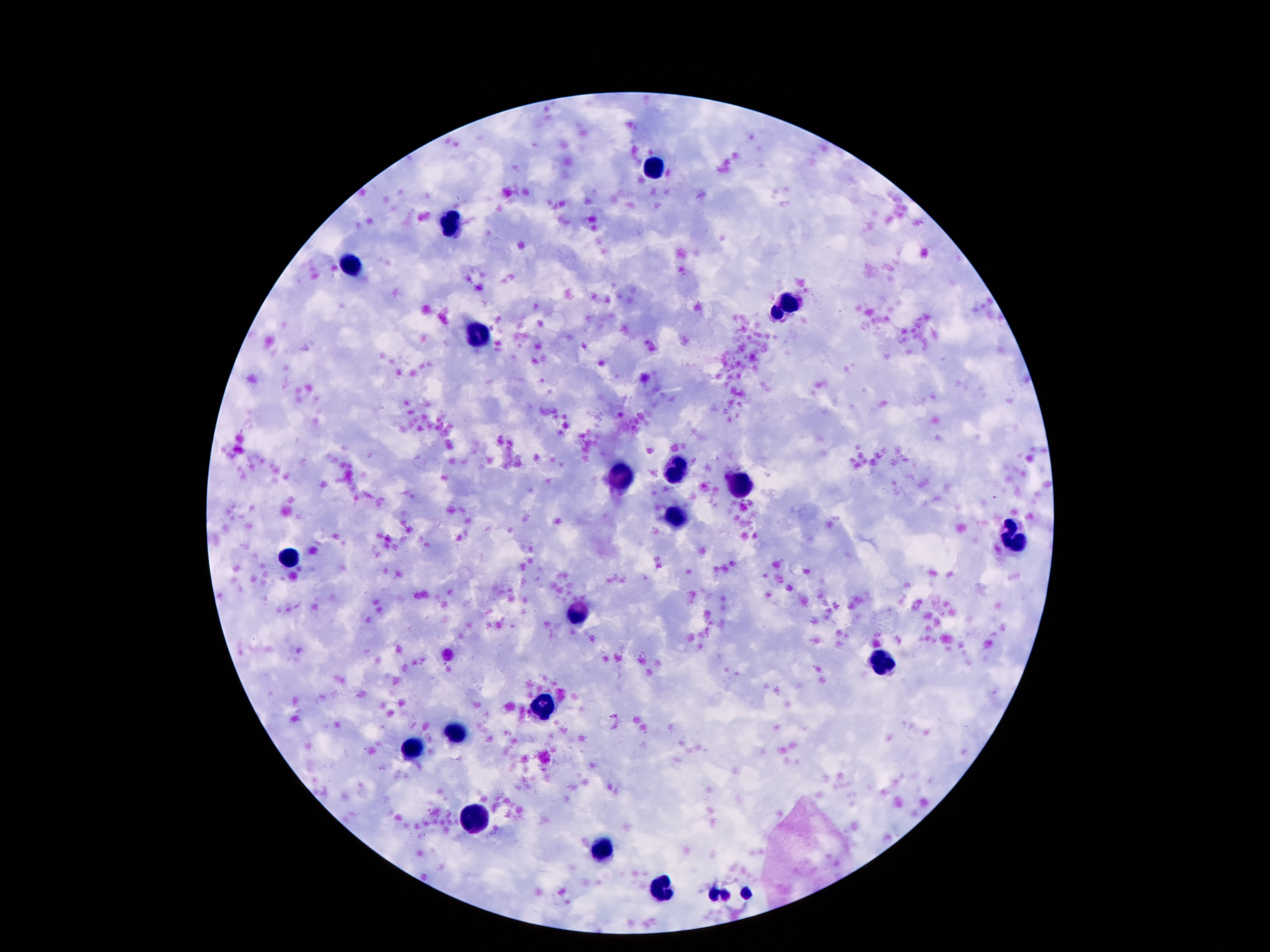 Approximate centers as (x, y) in pixels. Leukocyte locations: (654, 167), (451, 223), (351, 265), (783, 304), (477, 334), (678, 471), (623, 477), (738, 487), (674, 517), (1010, 539), (292, 557), (579, 611), (886, 664), (542, 706), (455, 734), (413, 750), (473, 820), (603, 847), (663, 887). One field from this slide. Thick peripheral-blood smear. Image is 1270×952 pixels. Smartphone photograph taken through the microscope eyepiece. 100x magnification. Giemsa-stained preparation. Patient malaria status: not infected.